State which cell type is depicted.
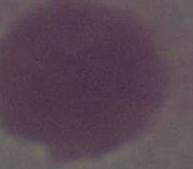

This is an erythrocyte.

Photomicrograph. 1000x magnification.